Classify this cell by malaria status.
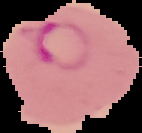

Parasitized.

From a thin blood smear. Segmented cell region on a black background. Image is 142×133 pixels.